Identify the parasite.
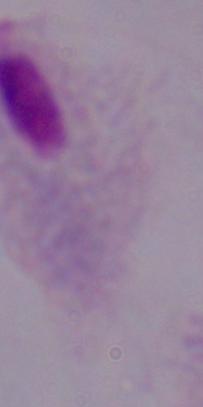
This is a trichomonad.

1000x magnification. Photomicrograph.